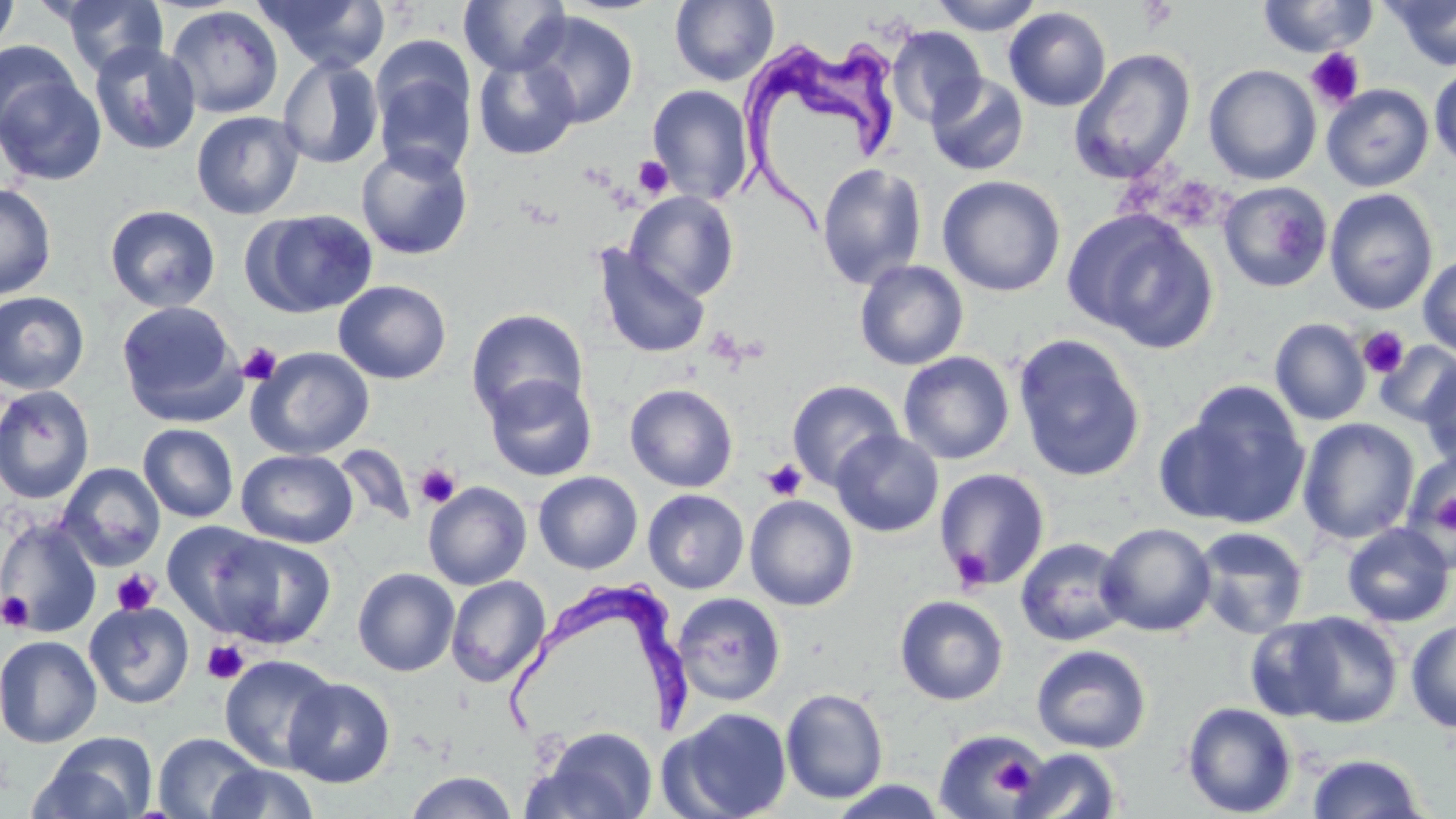

{
  "slide_level_diagnosis": "Trypanosoma brucei",
  "field_of_view": "one of a larger specimen",
  "magnification": "1000x",
  "trypanosoma_brucei_locations": "approximate bounding boxes as (x1,y1)-(x2,y2) corner pairs in pixels: (739,31)-(905,230), (500,580)-(693,746)",
  "uninfected_red_blood_cell_locations": "approximate bounding boxes as (x1,y1)-(x2,y2) corner pairs in pixels: (0,0)-(19,55), (55,0)-(170,78), (256,0)-(391,73), (458,0)-(572,76), (670,0)-(779,86), (929,0)-(1045,35), (1256,0)-(1380,58), (1383,0)-(1456,71), (166,5)-(284,118), (1004,7)-(1112,111), (523,11)-(639,128), (887,26)-(987,127), (0,39)-(81,141), (89,40)-(201,155), (1070,48)-(1196,184), (473,54)-(580,160), (277,56)-(384,169), (372,58)-(477,179), (1203,64)-(1322,186), (1429,65)-(1456,169), (0,70)-(107,186), (926,74)-(1029,176), (1321,83)-(1434,192), (646,85)-(755,204), (191,111)-(304,220), (355,143)-(473,260), (816,163)-(926,290), (937,175)-(1066,297), (1218,182)-(1333,293), (0,183)-(57,300), (1324,188)-(1438,315), (625,190)-(739,301), (104,204)-(221,312), (244,209)-(378,318), (1064,209)-(1219,352), (592,246)-(710,360), (1418,253)-(1456,358), (854,259)-(969,371), (333,280)-(452,384), (0,291)-(90,394), (116,301)-(243,425), (466,308)-(588,422), (1270,318)-(1371,426), (1012,333)-(1147,482), (1375,340)-(1456,426), (245,346)-(374,461), (898,351)-(1016,465), (1419,361)-(1455,470), (484,374)-(597,481), (787,380)-(904,490), (1161,382)-(1312,531), (624,383)-(738,492), (0,384)-(96,504), (1298,417)-(1419,545), (137,424)-(239,523), (830,429)-(944,538), (334,443)-(415,529), (236,449)-(358,549), (1403,452)-(1455,565), (56,462)-(166,571), (934,468)-(1050,590), (533,471)-(643,574), (423,481)-(532,590), (643,489)-(749,594), (745,495)-(859,611), (0,517)-(102,638), (162,520)-(274,634), (1097,522)-(1216,636), (1341,523)-(1455,627), (1193,527)-(1309,639), (210,533)-(338,649), (1015,537)-(1132,647), (352,567)-(459,676), (446,575)-(550,687), (673,592)-(786,706), (894,595)-(1009,705), (84,601)-(195,709), (1278,610)-(1404,728), (1243,616)-(1348,723), (1405,617)-(1456,733), (0,634)-(103,748), (1031,644)-(1151,753), (219,654)-(339,773), (283,677)-(396,788), (780,688)-(888,804), (1182,701)-(1297,818), (664,707)-(793,819), (532,725)-(659,819), (935,728)-(1044,819), (33,732)-(158,819), (152,732)-(265,819), (1009,748)-(1123,819), (1306,753)-(1426,818), (206,763)-(320,819), (404,771)-(517,818), (825,778)-(952,819)",
  "modality": "light microscopy",
  "image_size": "1456×819 pixels",
  "preparation": "thin blood smear",
  "stain": "May-Grünwald-Giemsa",
  "platelet_locations": "approximate bounding boxes as (x1,y1)-(x2,y2) corner pairs in pixels: (1305,47)-(1365,110), (633,156)-(674,199), (1357,327)-(1410,378), (238,343)-(282,385), (762,459)-(806,501), (415,463)-(461,508), (1432,486)-(1456,543), (948,546)-(993,592), (111,569)-(160,616), (1,591)-(34,632), (202,640)-(249,685), (989,751)-(1042,799)"
}